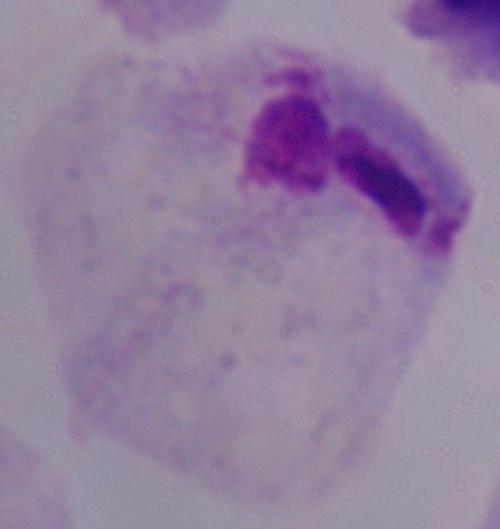
identification = trichomonad
magnification = 1000x
modality = micrograph